Report the malaria status of this cell.
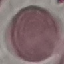
Uninfected.

preparation = thin blood smear
capture = smartphone through the microscope eyepiece
image type = automatically extracted cell patch, resized to 64 × 64 pixels
stain = Giemsa